Classify this cell by malaria status.
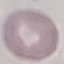

It is uninfected.

Giemsa-stained preparation. Automatically extracted cell patch, resized to 64 × 64 pixels. Photographed with a smartphone camera at the microscope eyepiece. Thin smear of blood.